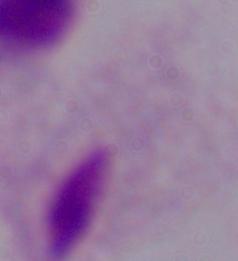

identification = trichomonad
magnification = 1000x
modality = photomicrograph